Point out each Plasmodium parasite.
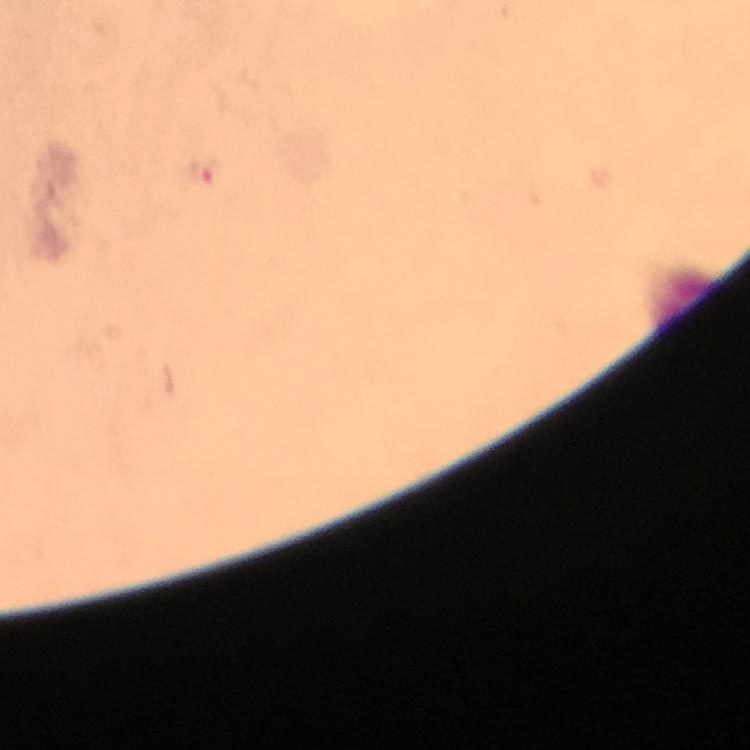
Approximate centers as [x, y] in pixels.
Plasmodium parasites: [200, 176].

Cropped region of a single field of view. 100x magnification. Immersion oil applied. Giemsa stain. Thick blood film. Photographed through the microscope with a smartphone camera. Image is 750×750 pixels. From a malaria diagnostic workup.